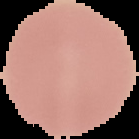

Image is 139×139 pixels. The area outside the segmented cell region is set to black. Result: no Plasmodium parasites seen. From a thin blood film.